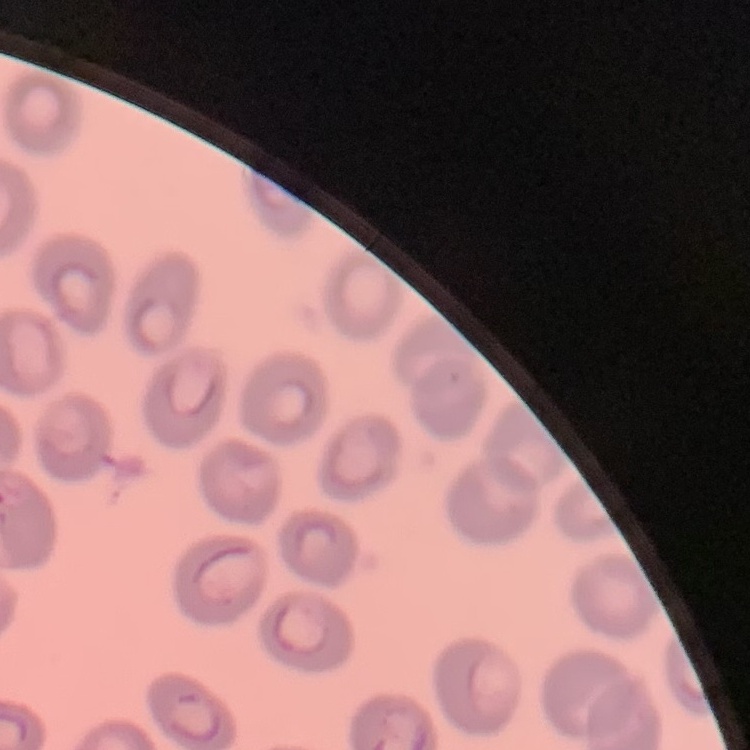
red blood cell morphology = no rouleaux formation
preparation = thin blood smear
image type = one tile cut from a larger photomicrograph
stain = Field's or Giemsa